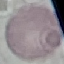

Malaria status: uninfected. Automatically extracted cell patch, resized to 64 × 64 pixels. Photographed with a smartphone camera at the microscope eyepiece. Giemsa stain. Thin blood smear.